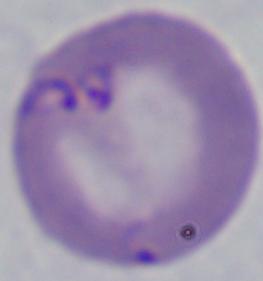
{
  "magnification": "1000x",
  "identification": "Babesia",
  "modality": "micrograph"
}